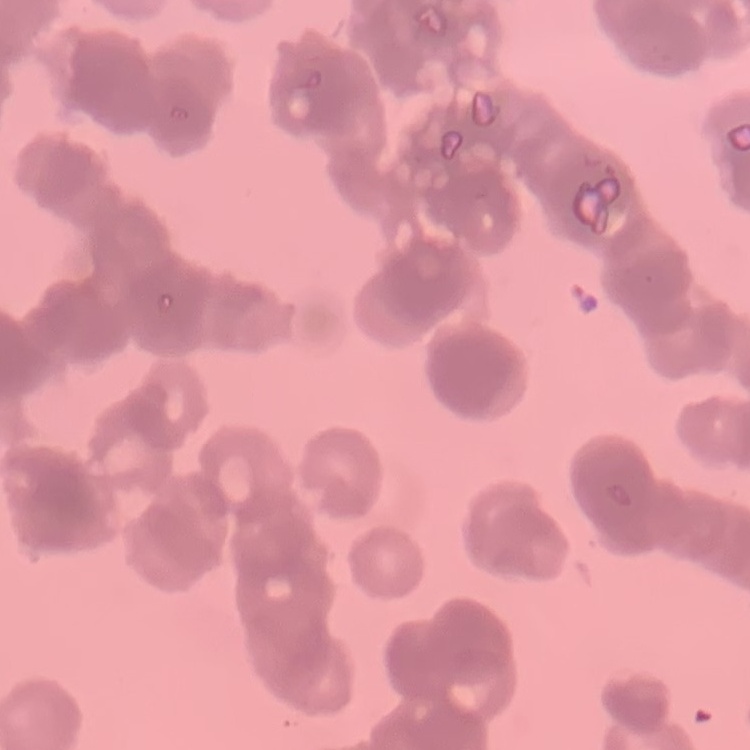

The red blood cells show rouleaux formation. Field's or Giemsa stain. One tile cut from a larger photomicrograph. Thin peripheral smear.